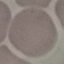

Malaria status: uninfected. Giemsa-stained preparation. Thin blood smear. Automatically extracted cell patch, resized to 64 × 64 pixels. Photographed with a smartphone camera at the microscope eyepiece.